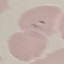

Result: malaria parasites detected. Giemsa-stained preparation. Acquired by smartphone through the microscope eyepiece. Cell patch, automatically extracted from a larger field of view and resized to 64 × 64 pixels. Thin blood film.